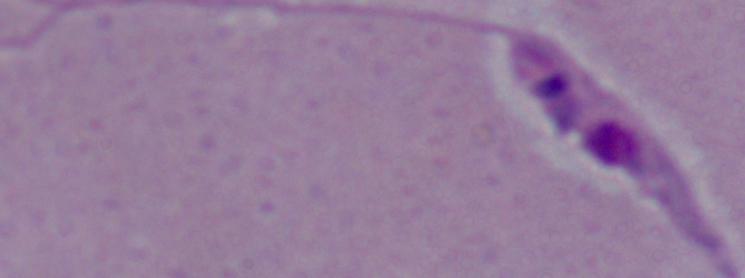
{
  "identification": "Leishmania",
  "magnification": "1000x",
  "modality": "micrograph"
}